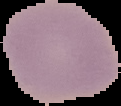

image_size: 121×106 pixels
malaria_status: uninfected
preparation: thin blood film
image_type: cell region segmented out of the field of view; surrounding area masked to black